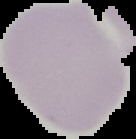

Summary:
  - Preparation: thin blood film
  - Image size: 136×139 pixels
  - Image type: segmented cell region with the area outside set to black
  - Result: negative for malaria parasites